Outline each blood parasite and name the species.
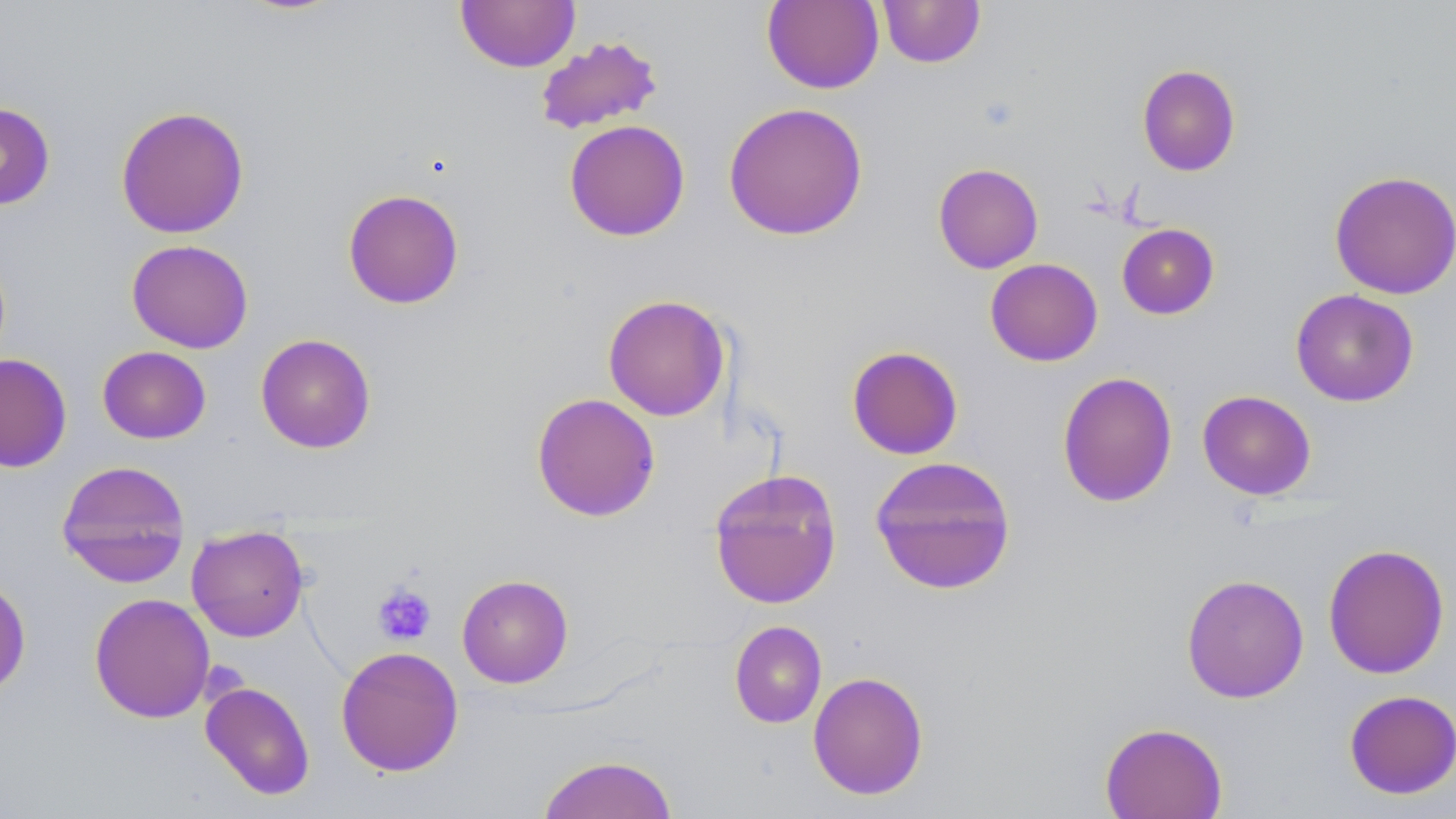
No blood parasites observed.

slide_level_diagnosis: negative for blood parasites
modality: light microscopy
uninfected_red_blood_cell_locations: 'approximate bounding boxes as (x1,y1)-(x2,y2) corner pairs in pixels: (877,0)-(986,69), (456,1)-(580,72), (762,1)-(884,94), (534,36)-(664,135), (1136,64)-(1241,176), (0,101)-(56,211), (723,101)-(868,241), (115,105)-(249,239), (564,119)-(690,241), (932,162)-(1044,273), (1329,170)-(1456,299), (342,188)-(465,309), (1116,223)-(1220,319), (126,239)-(253,353), (985,258)-(1103,366), (1290,289)-(1419,407), (602,294)-(731,421), (255,333)-(376,453), (846,345)-(964,460), (97,346)-(211,444), (0,353)-(72,472), (1057,371)-(1178,508), (1197,389)-(1317,501), (531,393)-(661,522), (869,455)-(1017,594), (56,460)-(191,587), (708,468)-(843,610), (186,525)-(309,642), (1322,543)-(1450,679), (1181,573)-(1309,703), (0,574)-(32,697), (457,574)-(573,688), (89,593)-(215,723), (729,620)-(827,728), (335,645)-(464,777), (807,670)-(929,800), (200,681)-(315,800), (1343,689)-(1456,799), (1099,721)-(1228,819), (536,754)-(680,818)'
field_of_view: single
platelet_locations: 'approximate bounding boxes as (x1,y1)-(x2,y2) corner pairs in pixels: (373,582)-(437,645)'
magnification: 1000x
stain: May-Grünwald-Giemsa
image_size: 1456×819 pixels
preparation: thin blood smear